Assess the morphology of the red blood cells.
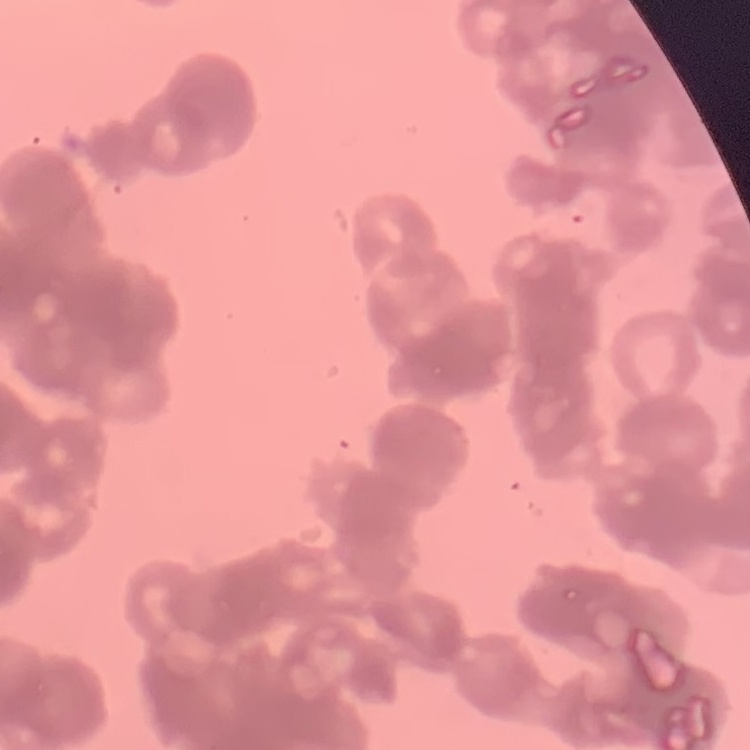

They show rouleaux formation.

Summary:
  - Preparation: thin blood film
  - Stain: Field's or Giemsa
  - Image type: square crop of a larger photomicrograph